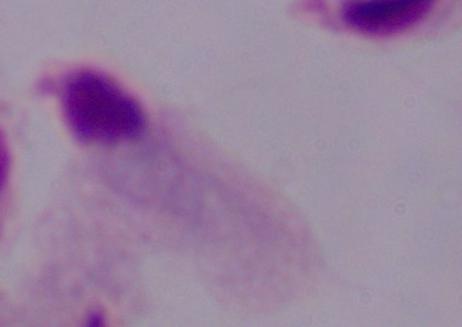

A trichomonad is seen. 1000x magnification. Micrograph.